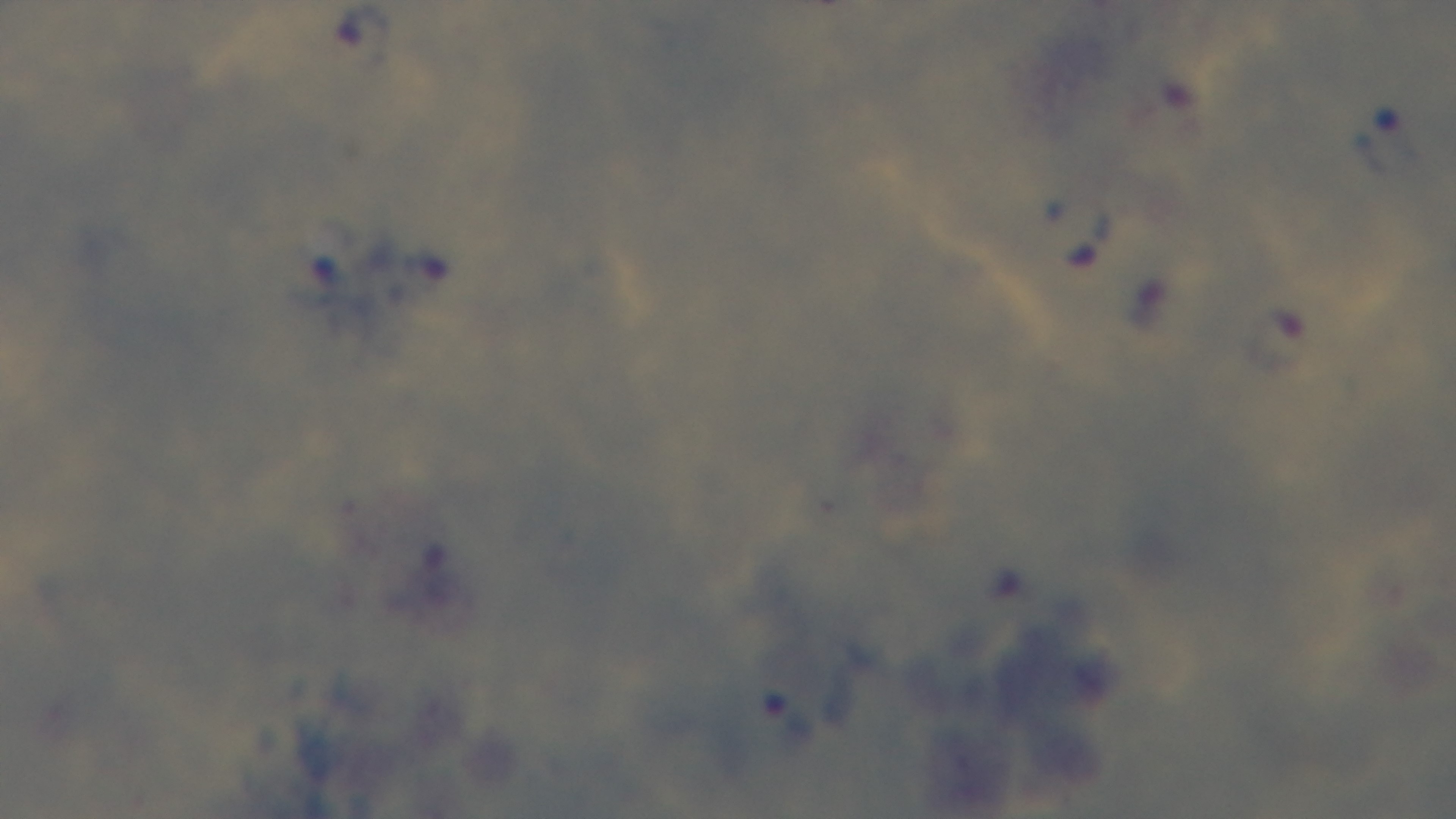

Summary:
  - Stain: Giemsa
  - Preparation: thick smear
  - Modality: light microscopy
  - Capture: mounted 4K digital camera
  - Objective: 100x oil immersion
  - Malaria status: positive
  - Field of view: single